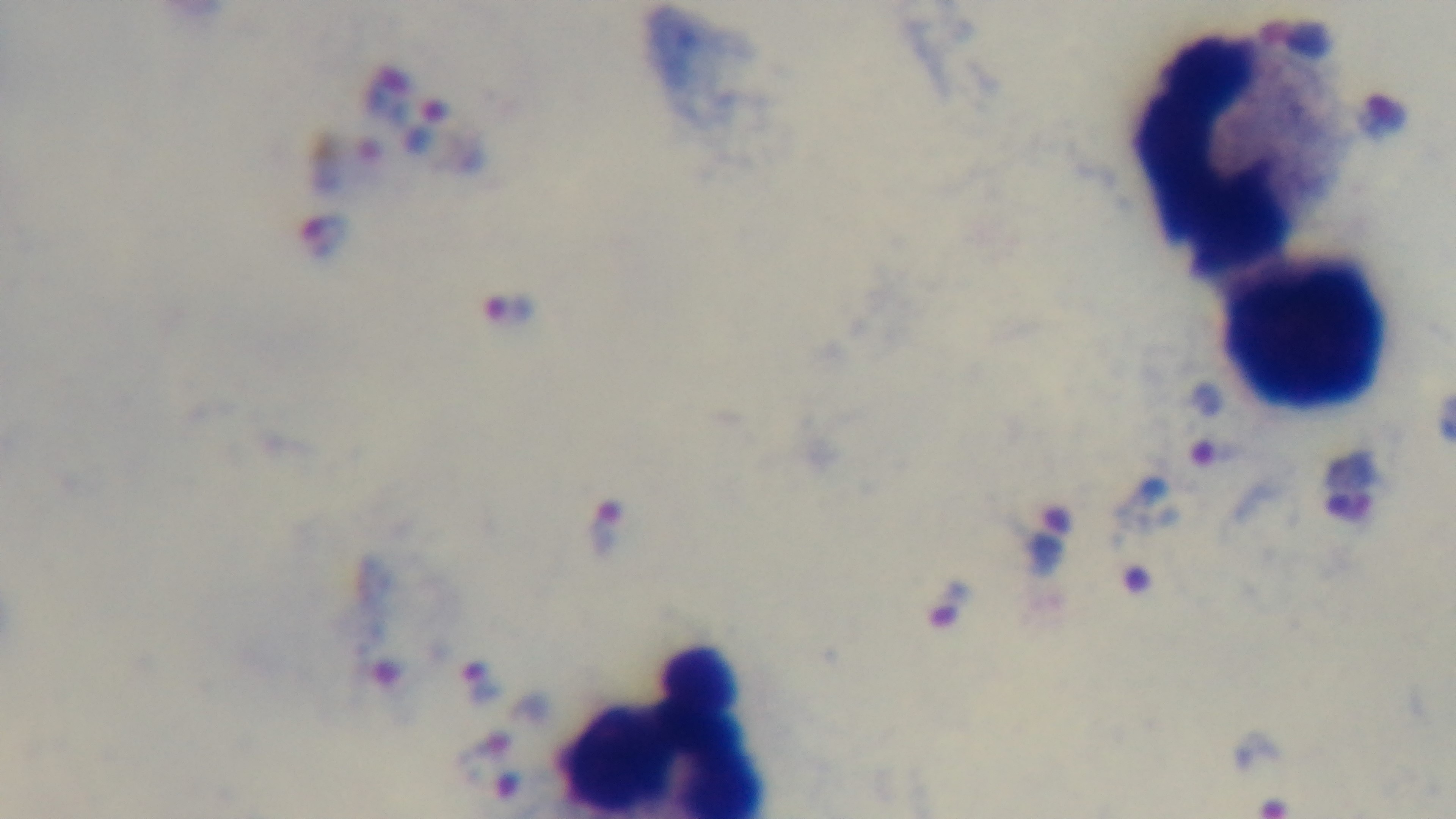 Oil-immersion objective, 100x. Malaria status: infected. Mounted 4K digital camera. Giemsa-stained. Preparation: thick. Single field of view. Photomicrograph.